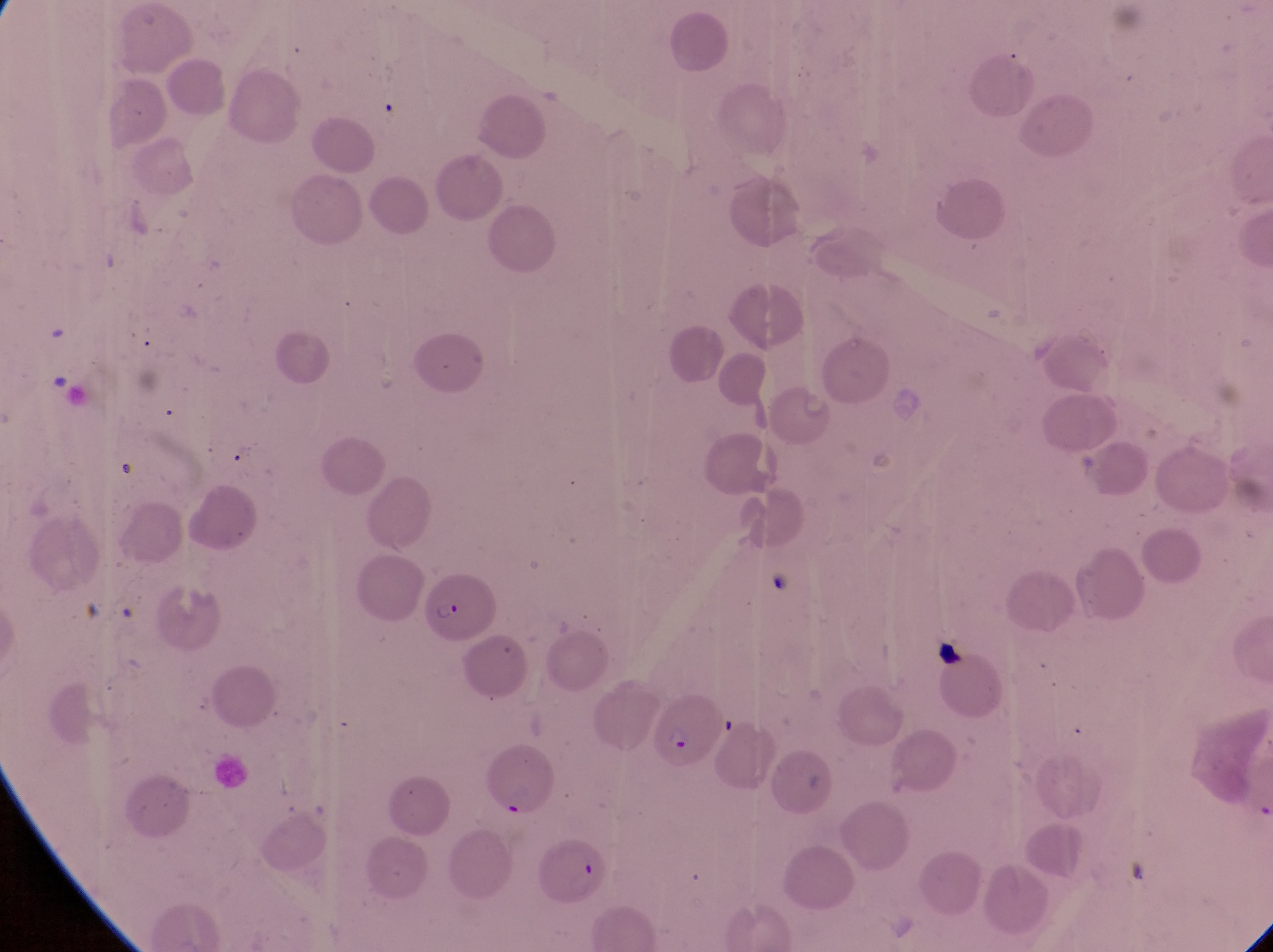

Approximate bounding boxes as left top right bottom in pixels. Artifact (platelet-like body, stain precipitate, or debris) locations: 932 633 964 667. Parasitised red blood cell locations: 424 570 496 640; 652 679 724 784; 530 834 610 911. One field of view. Magnification of 1000x. Photographed through the eyepiece of an Olympus CX-23 microscope with a smartphone camera. Thin blood film. Collected in Uganda. Image is 1273×952 pixels.